Comment on the morphology of the red blood cells.
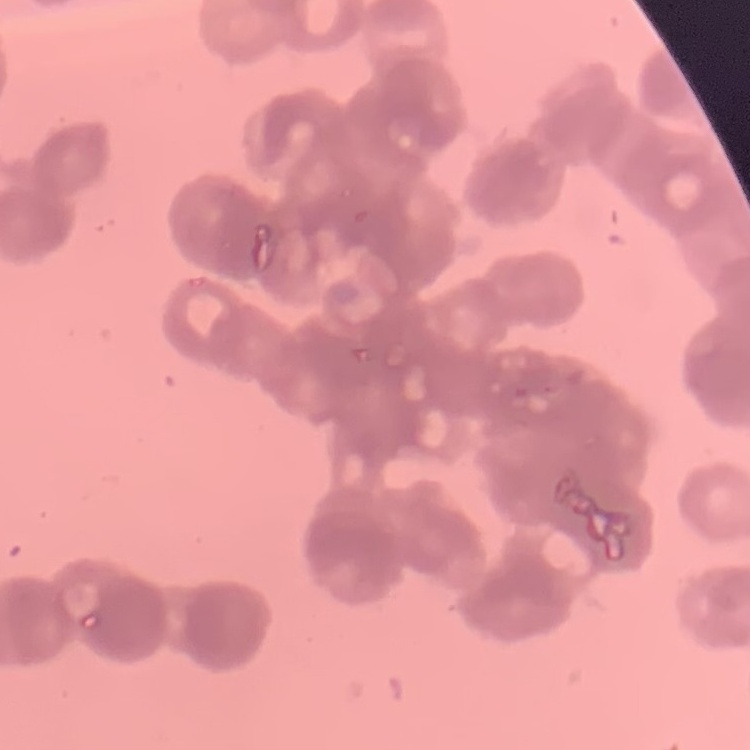
Rouleaux formation.

Thin peripheral smear. Stained with either Field's or Giemsa. Square crop of a larger photomicrograph.